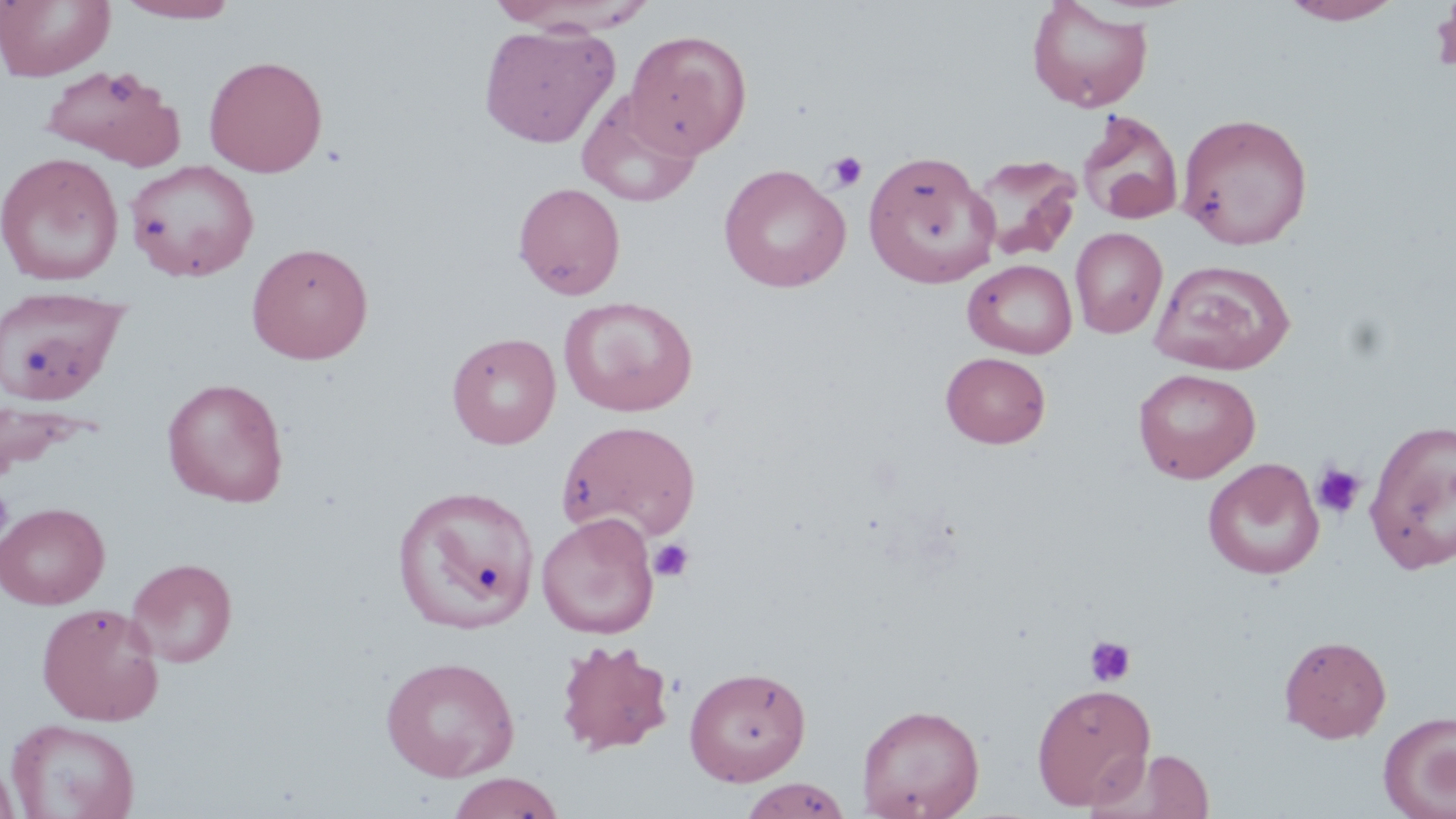

slide-level diagnosis = no evidence of blood parasites
uninfected red blood cell locations = approximate bounding boxes as named x1/y1/x2/y2 corners in pixels: (x1=0, y1=0, x2=115, y2=81), (x1=118, y1=0, x2=240, y2=23), (x1=1027, y1=0, x2=1153, y2=113), (x1=1282, y1=0, x2=1405, y2=25), (x1=478, y1=23, x2=619, y2=148), (x1=624, y1=29, x2=752, y2=159), (x1=204, y1=55, x2=328, y2=177), (x1=38, y1=63, x2=185, y2=168), (x1=577, y1=90, x2=704, y2=208), (x1=1077, y1=109, x2=1185, y2=226), (x1=1176, y1=112, x2=1313, y2=250), (x1=862, y1=151, x2=1000, y2=288), (x1=0, y1=152, x2=123, y2=287), (x1=968, y1=154, x2=1083, y2=262), (x1=125, y1=160, x2=259, y2=282), (x1=718, y1=163, x2=851, y2=293), (x1=513, y1=182, x2=626, y2=300), (x1=1070, y1=227, x2=1167, y2=338), (x1=246, y1=241, x2=374, y2=364), (x1=1149, y1=258, x2=1295, y2=375), (x1=963, y1=259, x2=1078, y2=359), (x1=0, y1=285, x2=129, y2=405), (x1=559, y1=296, x2=698, y2=416), (x1=447, y1=332, x2=561, y2=449), (x1=940, y1=351, x2=1051, y2=448), (x1=1133, y1=368, x2=1260, y2=483), (x1=162, y1=377, x2=289, y2=508), (x1=0, y1=398, x2=87, y2=479), (x1=1363, y1=418, x2=1456, y2=574), (x1=556, y1=419, x2=701, y2=542), (x1=1203, y1=458, x2=1324, y2=580), (x1=393, y1=483, x2=539, y2=633), (x1=0, y1=502, x2=110, y2=609), (x1=536, y1=512, x2=660, y2=639), (x1=126, y1=557, x2=238, y2=668), (x1=36, y1=601, x2=164, y2=725), (x1=1279, y1=634, x2=1392, y2=743), (x1=555, y1=639, x2=675, y2=756), (x1=380, y1=655, x2=521, y2=782), (x1=683, y1=665, x2=811, y2=786), (x1=1031, y1=682, x2=1156, y2=810), (x1=857, y1=702, x2=985, y2=819), (x1=1378, y1=711, x2=1456, y2=818), (x1=6, y1=718, x2=140, y2=819), (x1=1090, y1=747, x2=1218, y2=818), (x1=0, y1=758, x2=19, y2=819), (x1=446, y1=772, x2=565, y2=818), (x1=739, y1=777, x2=852, y2=818)
stain = May-Grünwald-Giemsa
field of view = one of a larger specimen
platelet locations = approximate bounding boxes as named x1/y1/x2/y2 corners in pixels: (x1=105, y1=69, x2=140, y2=104), (x1=827, y1=151, x2=868, y2=192), (x1=1310, y1=462, x2=1366, y2=520), (x1=0, y1=484, x2=14, y2=541), (x1=649, y1=538, x2=694, y2=583), (x1=1083, y1=635, x2=1137, y2=688)
image size = 1456×819 pixels
modality = light microscopy
preparation = thin blood film
magnification = 1000x